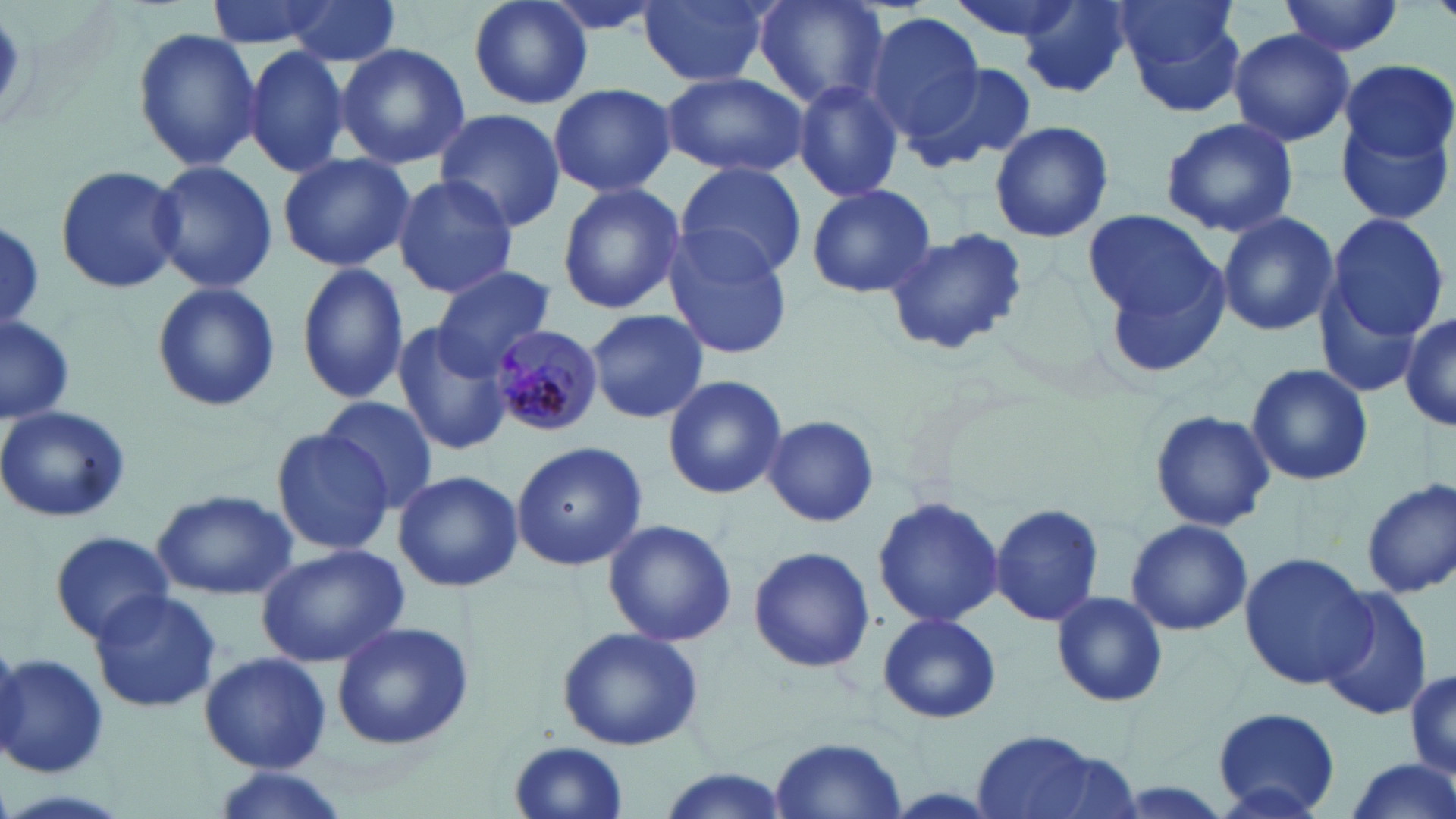
Summary:
  - Coordinate format: approximate bounding boxes as (x1,y1)-(x2,y2) corner pairs in pixels
  - Plasmodium malariae-infected red blood cell locations: (489,323)-(604,435)
  - Uninfected red blood cell locations: (204,0)-(343,49), (280,0)-(403,67), (467,0)-(594,112), (535,0)-(673,38), (639,0)-(771,87), (752,0)-(889,110), (1111,0)-(1246,107), (1280,0)-(1403,59), (1017,2)-(1135,98), (867,11)-(986,141), (131,25)-(263,172), (1227,28)-(1355,145), (243,43)-(349,179), (335,43)-(470,170), (1197,47)-(1337,204), (1340,59)-(1454,166), (908,62)-(1036,173), (662,71)-(809,178), (792,79)-(904,202), (548,82)-(676,198), (1334,101)-(1455,230), (435,107)-(565,232), (1160,117)-(1301,239), (989,120)-(1115,242), (277,153)-(415,272), (145,161)-(281,294), (675,161)-(806,279), (55,166)-(186,293), (391,174)-(518,298), (556,181)-(685,315), (803,182)-(938,300), (1083,210)-(1220,321), (1217,211)-(1338,337), (1321,211)-(1450,350), (1,221)-(44,333), (881,224)-(1030,359), (661,228)-(795,358), (1095,244)-(1235,385), (295,263)-(408,403), (432,265)-(554,374), (150,280)-(280,414), (584,308)-(708,425), (0,311)-(78,426), (1402,312)-(1456,433), (391,323)-(516,456), (1244,361)-(1375,487), (661,374)-(787,500), (319,397)-(439,511), (0,404)-(132,525), (1148,409)-(1276,533), (763,415)-(880,529), (268,425)-(395,557), (511,441)-(648,571), (392,469)-(522,593), (1361,478)-(1456,599), (153,489)-(297,601), (872,495)-(1004,628), (989,503)-(1104,628), (602,518)-(737,648), (1125,518)-(1252,637), (49,530)-(173,643), (256,544)-(410,668), (747,545)-(874,673), (1238,553)-(1375,689), (1318,588)-(1435,721), (87,591)-(222,714), (1050,591)-(1169,708), (877,610)-(1002,726), (329,621)-(473,750), (556,624)-(703,753), (0,651)-(110,777), (198,651)-(332,773), (1407,667)-(1456,782), (1211,707)-(1342,818), (959,731)-(1135,819), (769,737)-(908,817), (508,742)-(630,819), (1340,761)-(1456,819), (203,766)-(353,819), (652,767)-(791,819)
  - Slide-level diagnosis: Plasmodium malariae
  - Stain: May-Grünwald-Giemsa
  - Magnification: 1000x
  - Preparation: thin blood smear
  - Modality: light microscopy
  - Field of view: single
  - Image size: 1456×819 pixels